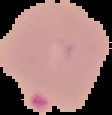
preparation = thin blood smear
image type = segmented cell region with the area outside set to black
image size = 112×115 pixels
malaria status = parasitized